Assess this cell for malaria.
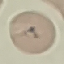

It is uninfected.

Cell patch, automatically extracted from a larger field of view and resized to 64 × 64 pixels. Thin blood film. Giemsa stain. Acquired by smartphone through the microscope eyepiece.